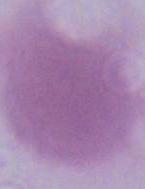
Summary:
  - Identification: erythrocyte
  - Modality: micrograph
  - Magnification: 1000x